Report the malaria status of this cell.
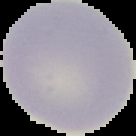

Uninfected.

The area outside the segmented cell region is set to black. Image is 136×136 pixels. From a thin blood film.